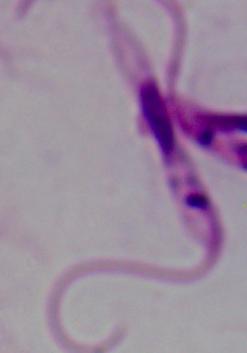

Summary:
  - Magnification: 1000x
  - Identification: Leishmania
  - Modality: micrograph